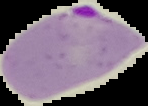

Summary:
  - Preparation: thin blood film
  - Result: malaria parasites identified
  - Image type: segmented cell region with the area outside set to black
  - Image size: 148×106 pixels